Report the malaria status of this cell.
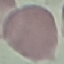

It is uninfected.

Photographed with a smartphone camera at the microscope eyepiece. Giemsa stain. Cell patch, automatically extracted from a larger field of view and resized to 64 × 64 pixels. Thin smear of blood.